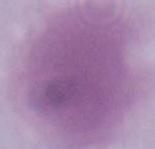 Photomicrograph. 1000x magnification. A red blood cell is seen.